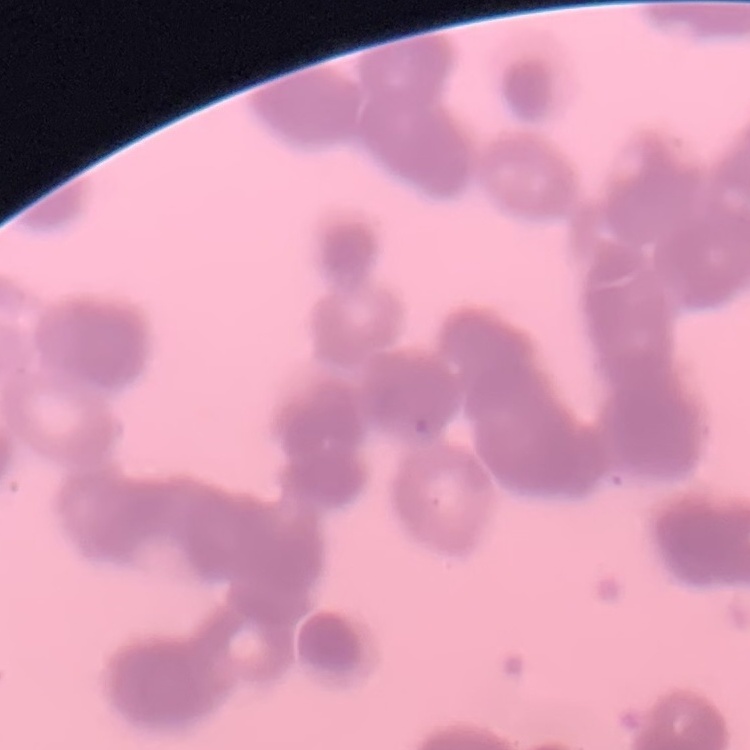
The erythrocytes show rouleaux formation. One tile cut from a larger photomicrograph. Thin peripheral smear. Field's or Giemsa stain.